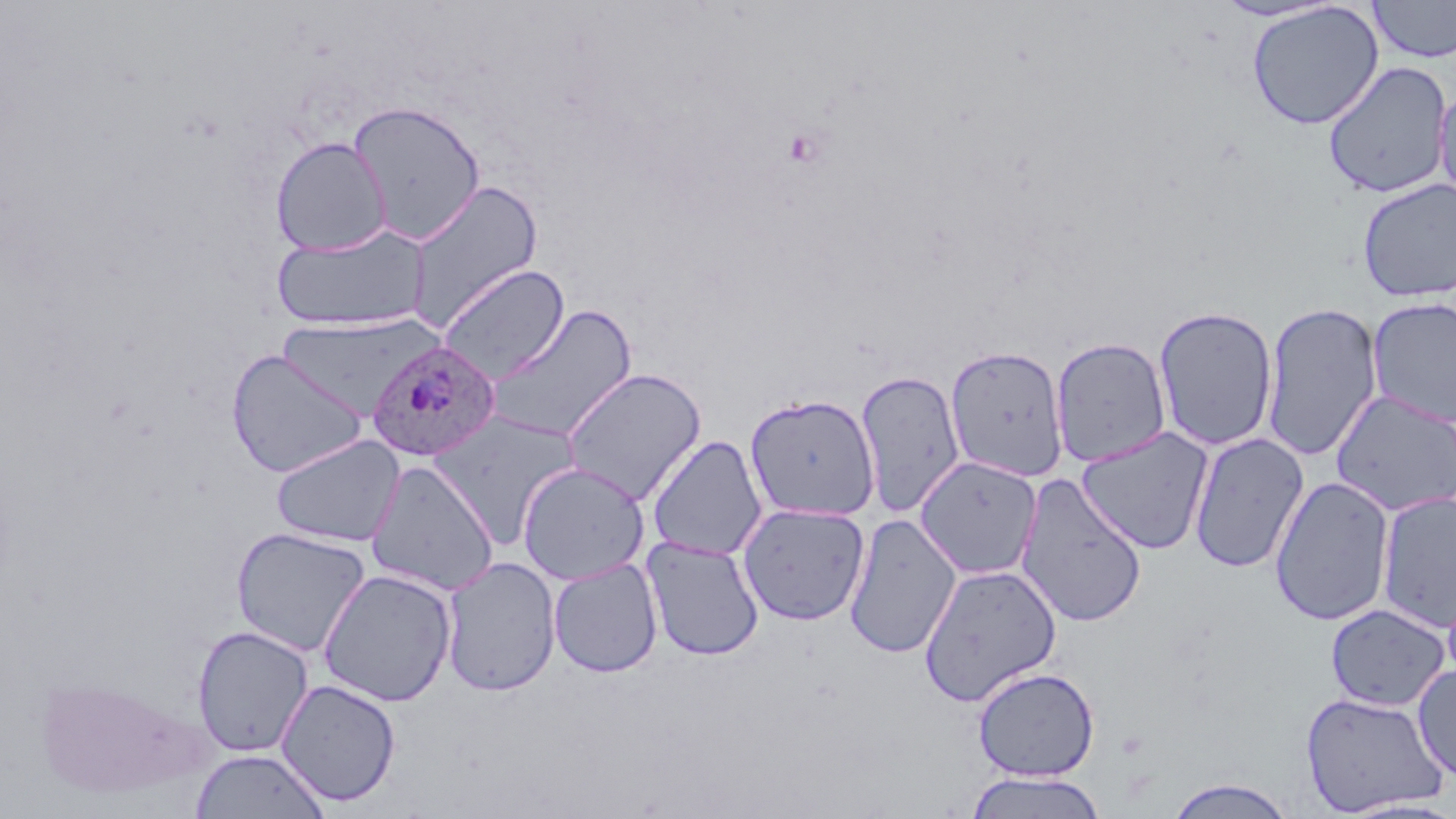
Summary:
  - Coordinate format: approximate bounding boxes as (x1,y1)-(x2,y2) corner pairs in pixels
  - Plasmodium ovale-infected red blood cell locations: (367,340)-(499,462)
  - Uninfected red blood cell locations: (1368,0)-(1456,63), (1246,2)-(1384,130), (1322,61)-(1453,199), (1433,82)-(1456,212), (347,100)-(486,244), (270,136)-(391,255), (406,178)-(543,334), (1356,178)-(1456,303), (270,224)-(430,333), (438,263)-(569,384), (1366,296)-(1456,427), (1260,301)-(1384,462), (486,304)-(637,443), (1153,305)-(1279,452), (277,314)-(437,421), (1050,336)-(1172,467), (944,344)-(1070,482), (226,349)-(369,478), (561,367)-(706,506), (855,370)-(965,518), (1330,388)-(1456,517), (745,393)-(880,521), (430,411)-(583,542), (1075,426)-(1215,555), (1189,432)-(1309,574), (270,434)-(404,547), (646,435)-(767,560), (915,456)-(1042,579), (366,460)-(499,595), (516,461)-(650,585), (1015,473)-(1147,628), (1269,475)-(1395,626), (1377,490)-(1456,634), (737,502)-(871,626), (843,513)-(962,659), (230,526)-(372,658), (642,536)-(763,661), (441,556)-(561,697), (548,557)-(663,678), (918,562)-(1062,707), (318,568)-(457,707), (1326,603)-(1451,712), (192,625)-(314,757), (1413,664)-(1456,784), (972,666)-(1099,781), (35,674)-(196,800), (276,678)-(401,806), (1299,691)-(1451,816), (189,748)-(331,819), (963,771)-(1109,819), (1165,776)-(1296,818)
  - Slide-level diagnosis: Plasmodium ovale
  - Image size: 1456×819 pixels
  - Stain: May-Grünwald-Giemsa
  - Preparation: thin blood smear
  - Field of view: one of a larger specimen
  - Magnification: 1000x
  - Modality: optical microscopy